Report the malaria status of this cell.
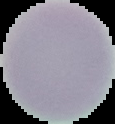

Uninfected.

Segmented cell region on a black background. Image is 115×124 pixels. From a thin blood film.